Name the parasite shown.
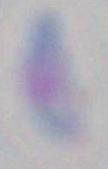

Toxoplasma gondii.

Summary:
  - Magnification: 1000x
  - Modality: photomicrograph